Report the malaria status of this cell.
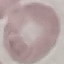
Uninfected.

Automatically extracted cell patch, resized to 64 × 64 pixels. Thin blood smear. Giemsa stain. Photographed with a smartphone camera at the microscope eyepiece.